Identify the parasite.
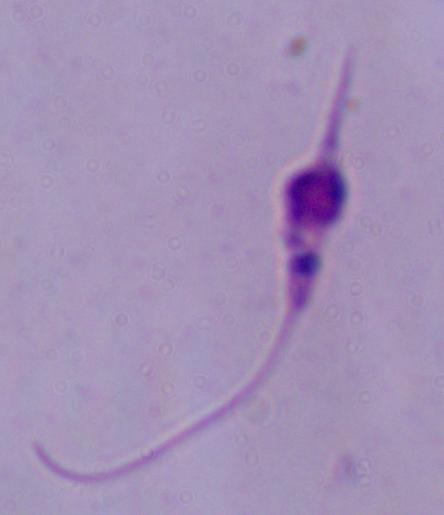

Leishmania.

Captured at 1000x magnification. Photomicrograph.